Classify this cell by malaria status.
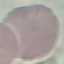
Uninfected.

{
  "image_type": "automatically extracted cell patch, resized to 64 × 64 pixels",
  "preparation": "thin blood smear",
  "stain": "Giemsa",
  "capture": "smartphone camera at the microscope eyepiece"
}